Outline each Plasmodium falciparum-infected red blood cell.
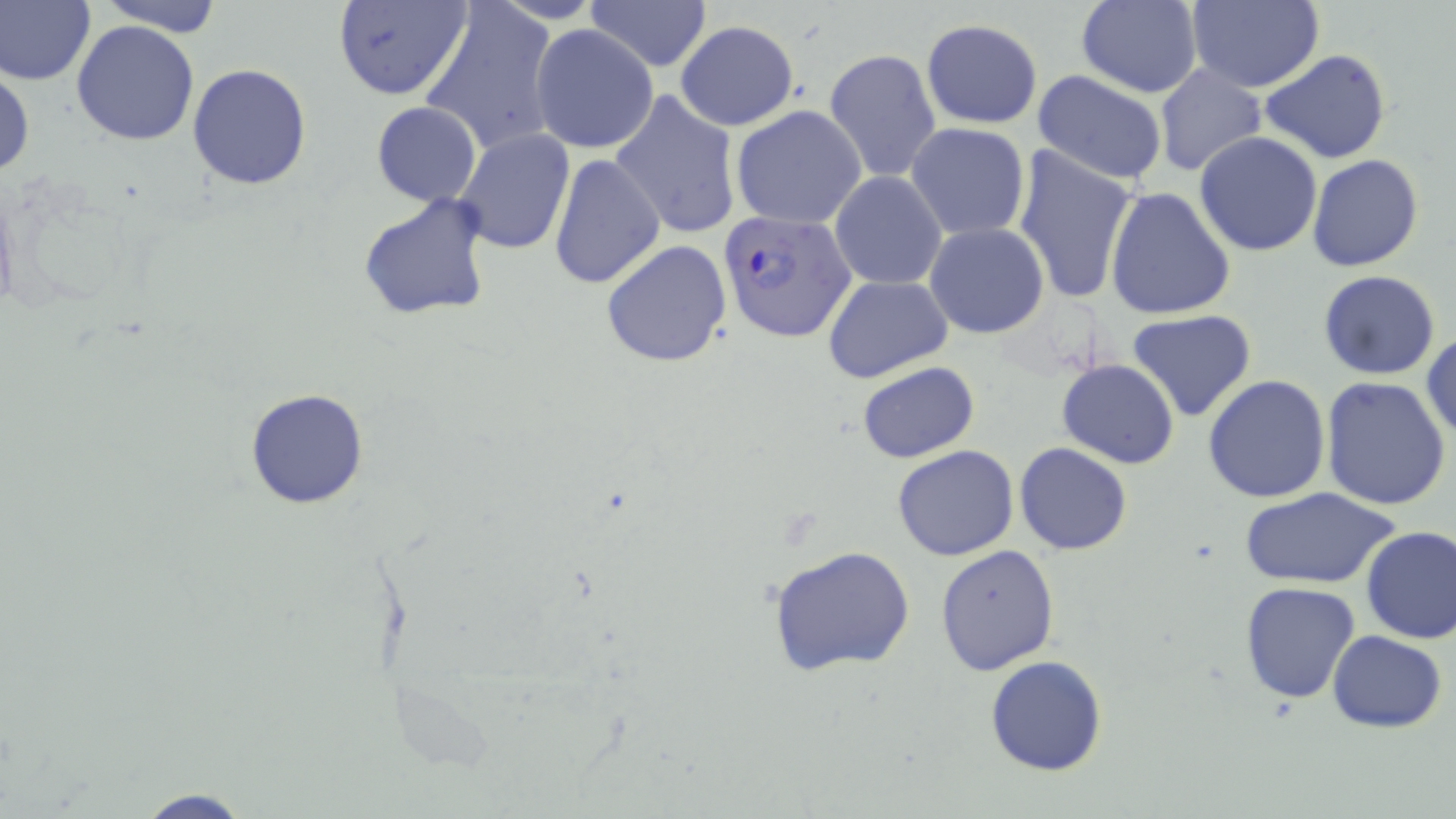

Approximate bounding boxes as named x1/y1/x2/y2 corners in pixels.
Plasmodium falciparum-infected red blood cells: (x1=718, y1=210, x2=857, y2=343).

slide-level diagnosis = Plasmodium falciparum
image size = 1456×819 pixels
uninfected red blood cell locations = approximate bounding boxes as named x1/y1/x2/y2 corners in pixels: (x1=0, y1=0, x2=96, y2=87), (x1=97, y1=0, x2=225, y2=34), (x1=332, y1=0, x2=471, y2=103), (x1=585, y1=0, x2=711, y2=73), (x1=1183, y1=0, x2=1325, y2=92), (x1=420, y1=1, x2=559, y2=158), (x1=1074, y1=1, x2=1203, y2=97), (x1=921, y1=19, x2=1042, y2=129), (x1=72, y1=20, x2=201, y2=146), (x1=676, y1=20, x2=799, y2=130), (x1=530, y1=24, x2=657, y2=153), (x1=825, y1=48, x2=941, y2=184), (x1=1261, y1=49, x2=1389, y2=164), (x1=0, y1=61, x2=35, y2=181), (x1=188, y1=62, x2=311, y2=191), (x1=1155, y1=64, x2=1266, y2=176), (x1=1031, y1=71, x2=1169, y2=185), (x1=612, y1=90, x2=742, y2=240), (x1=370, y1=102, x2=481, y2=207), (x1=731, y1=105, x2=868, y2=229), (x1=906, y1=121, x2=1032, y2=241), (x1=453, y1=128, x2=575, y2=254), (x1=1194, y1=132, x2=1324, y2=257), (x1=1012, y1=145, x2=1139, y2=307), (x1=549, y1=154, x2=665, y2=290), (x1=1306, y1=155, x2=1426, y2=272), (x1=830, y1=171, x2=947, y2=290), (x1=1104, y1=188, x2=1237, y2=319), (x1=358, y1=194, x2=493, y2=320), (x1=924, y1=222, x2=1049, y2=339), (x1=600, y1=239, x2=733, y2=368), (x1=1317, y1=270, x2=1440, y2=380), (x1=824, y1=273, x2=952, y2=383), (x1=1126, y1=309, x2=1258, y2=423), (x1=1421, y1=331, x2=1455, y2=443), (x1=1057, y1=358, x2=1179, y2=470), (x1=858, y1=361, x2=979, y2=463), (x1=1203, y1=375, x2=1332, y2=504), (x1=1320, y1=376, x2=1454, y2=510), (x1=246, y1=388, x2=369, y2=509), (x1=1015, y1=442, x2=1132, y2=556), (x1=893, y1=446, x2=1019, y2=561), (x1=1241, y1=486, x2=1398, y2=589), (x1=1359, y1=524, x2=1456, y2=644), (x1=935, y1=544, x2=1060, y2=677), (x1=767, y1=545, x2=917, y2=677), (x1=1239, y1=581, x2=1362, y2=703), (x1=1327, y1=631, x2=1446, y2=732), (x1=985, y1=655, x2=1108, y2=775), (x1=126, y1=789, x2=261, y2=818)
modality = optical microscopy
field of view = single
magnification = 1000x
preparation = thin blood film
stain = May-Grünwald-Giemsa